Assess the morphology of the erythrocytes.
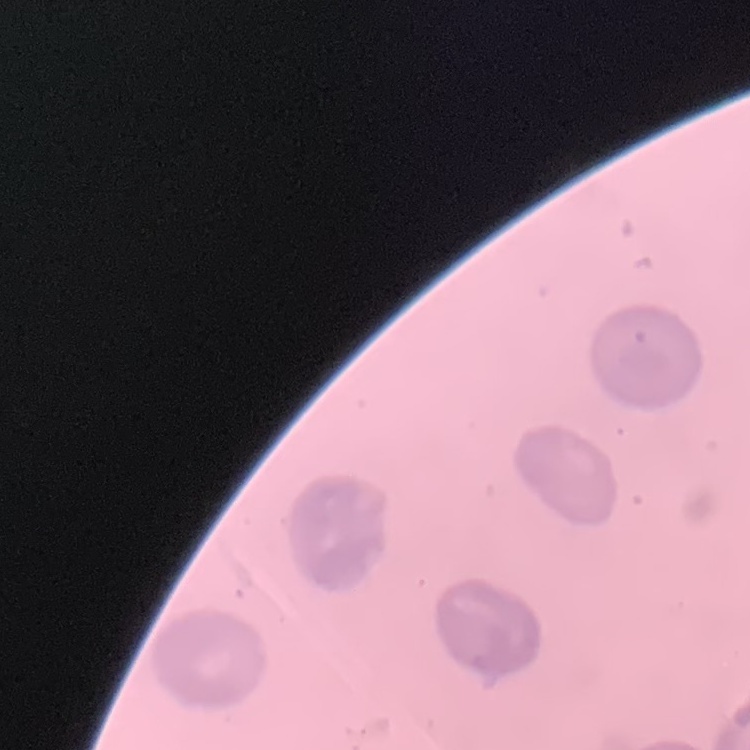

They show no rouleaux formation.

Summary:
  - Preparation: thin peripheral smear
  - Stain: Field's or Giemsa
  - Image type: one tile cut from a larger photomicrograph